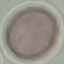
Summary:
  - Malaria status: uninfected
  - Capture: smartphone camera at the microscope eyepiece
  - Stain: Giemsa
  - Preparation: thin blood film
  - Image type: cell patch, automatically extracted from a larger field of view and resized to 64 × 64 pixels